Point out each leukocyte.
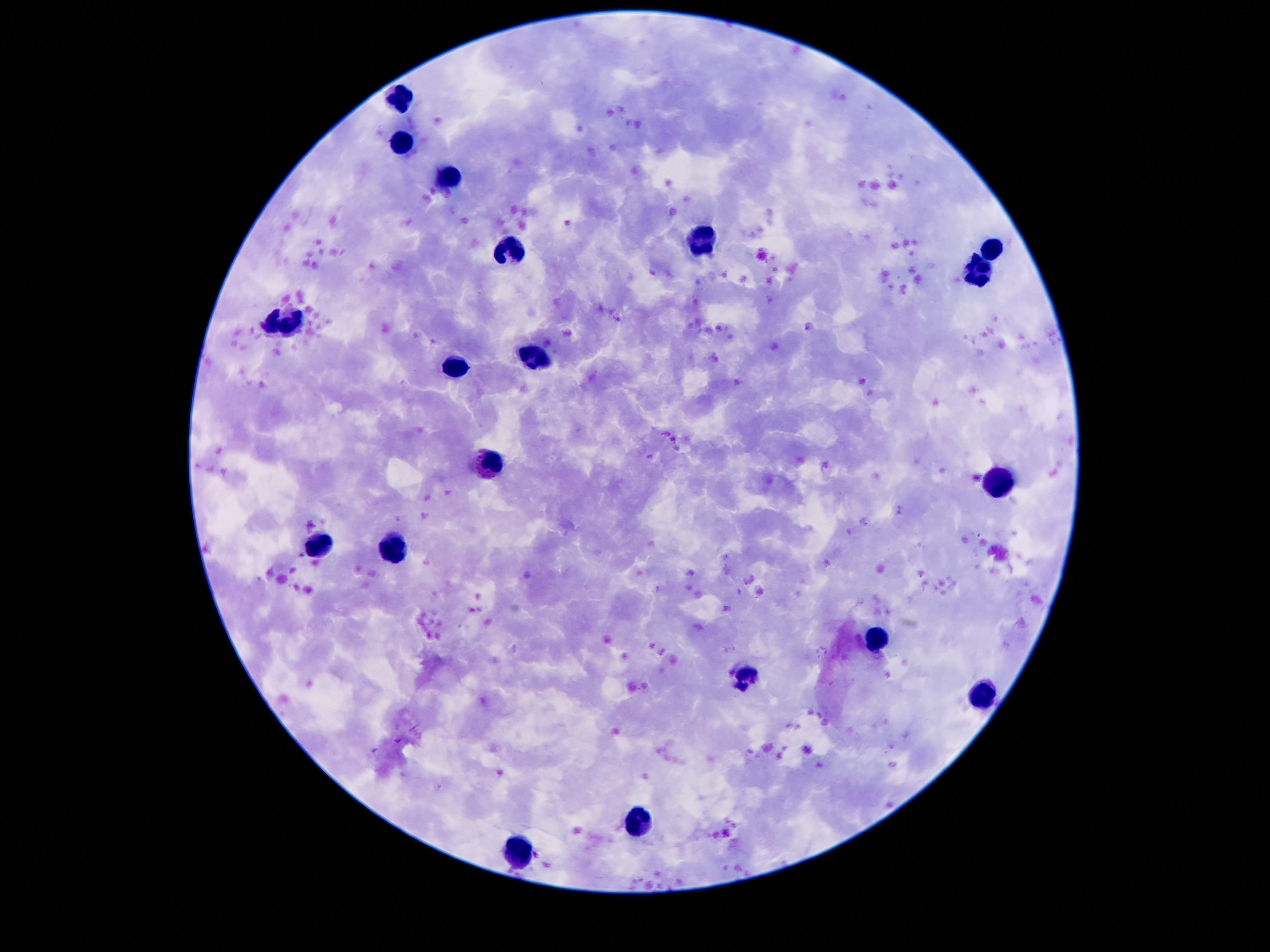

Approximate object centers, in pixels from the top-left corner.
Leukocytes: (x=401, y=97), (x=403, y=139), (x=445, y=179), (x=699, y=242), (x=993, y=248), (x=506, y=250), (x=980, y=275), (x=281, y=325), (x=539, y=355), (x=456, y=368), (x=489, y=466), (x=997, y=481), (x=321, y=544), (x=392, y=548), (x=879, y=638), (x=747, y=676), (x=985, y=695), (x=636, y=821), (x=519, y=851).

Summary:
  - Magnification: 100x
  - Capture: smartphone camera through the microscope eyepiece
  - Image size: 1270×952 pixels
  - Patient malaria status: uninfected
  - Stain: Giemsa
  - Field of view: one from this slide
  - Preparation: thick peripheral-blood smear